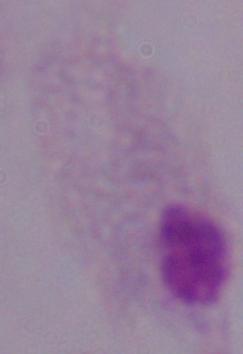
modality = photomicrograph
identification = trichomonad
magnification = 1000x